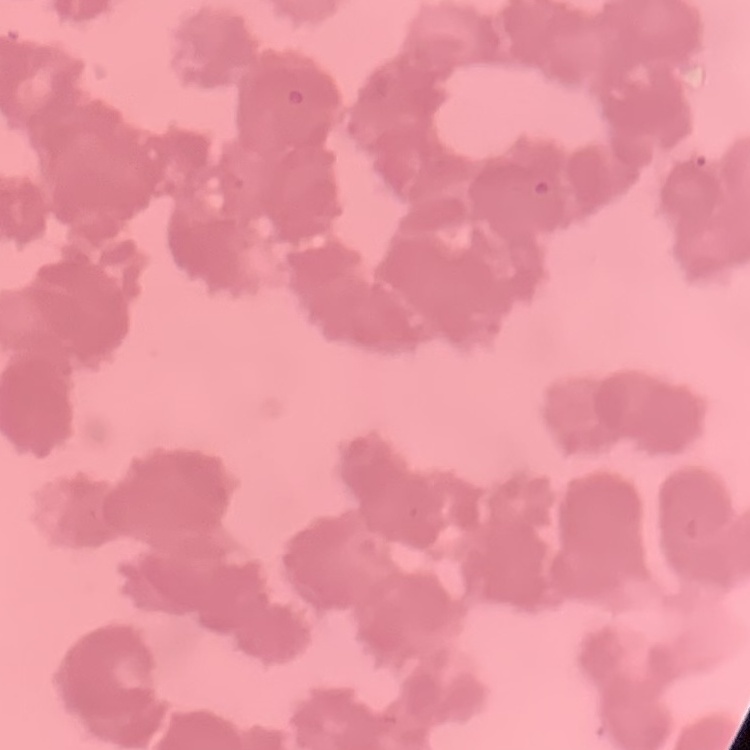

erythrocyte morphology = rouleaux formation
stain = Field's or Giemsa
image type = square crop of a larger photomicrograph
preparation = thin blood film